Report the malaria status of this cell.
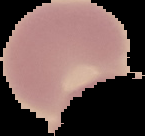
It is uninfected.

Summary:
  - Image type: segmented cell region with the area outside set to black
  - Preparation: thin blood film
  - Image size: 145×136 pixels